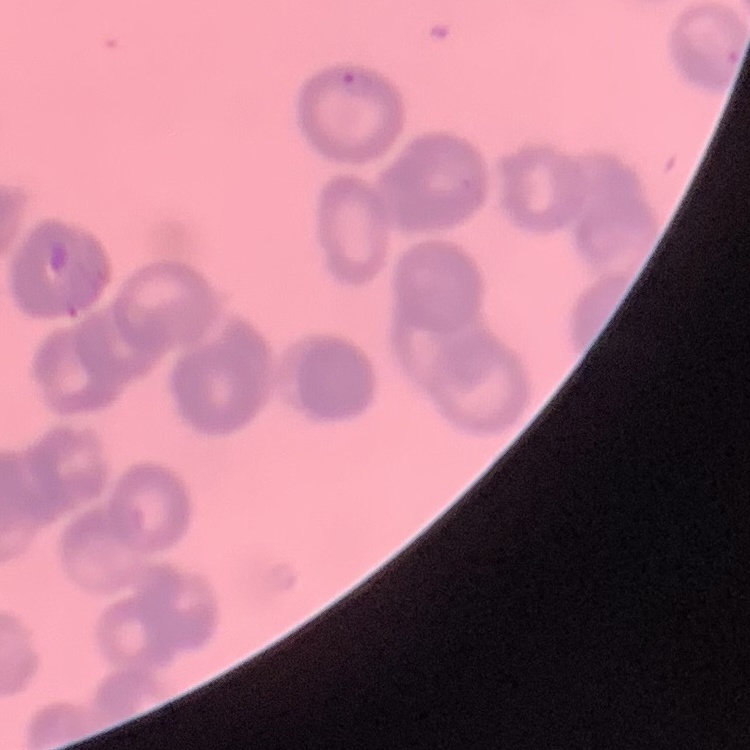
{
  "erythrocyte_morphology": "rouleaux formation",
  "stain": "Field's or Giemsa",
  "image_type": "one tile cut from a larger photomicrograph",
  "preparation": "thin blood smear"
}